Report the malaria status of this cell.
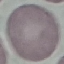

Uninfected.

{
  "preparation": "thin blood film",
  "image_type": "cell patch, automatically extracted from a larger field of view and resized to 64 × 64 pixels",
  "capture": "smartphone camera at the microscope eyepiece",
  "stain": "Giemsa"
}